Locate every leukocyte (white blood cell).
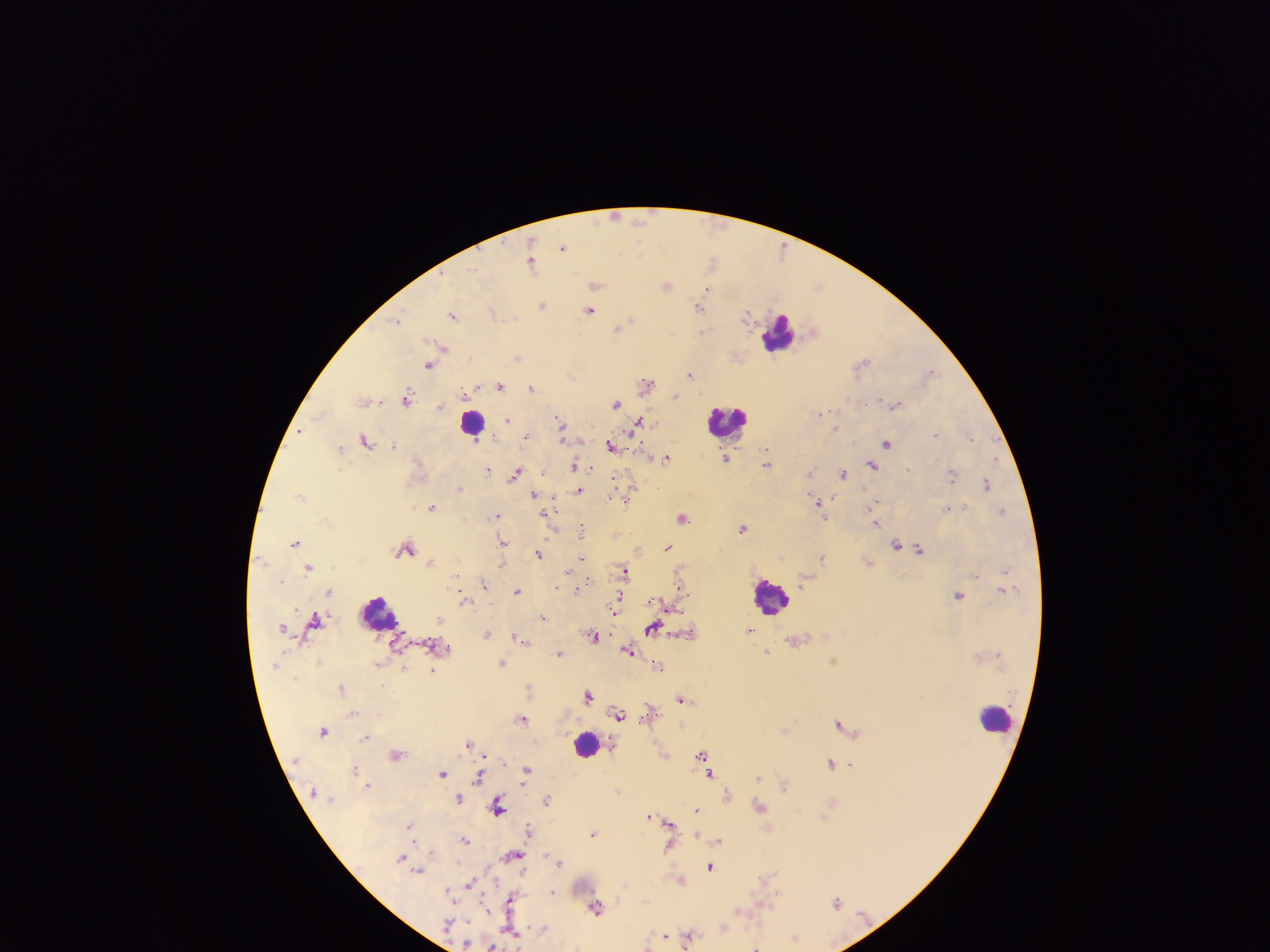

Approximate centers as {x, y} in pixels.
Leukocytes: {780, 333}, {728, 420}, {472, 422}, {770, 596}, {378, 613}, {995, 717}, {585, 744}.

Summary:
  - Plasmodium parasite locations: {616, 215}, {641, 219}, {563, 247}, {641, 252}, {713, 260}, {532, 261}, {595, 285}, {819, 285}, {667, 286}, {708, 289}, {542, 305}, {699, 307}, {589, 310}, {492, 312}, {747, 314}, {453, 315}, {397, 319}, {619, 328}, {704, 330}, {442, 347}, {518, 358}, {862, 362}, {428, 365}, {931, 372}, {690, 373}, {572, 375}, {646, 383}, {500, 386}, {532, 387}, {676, 396}, {408, 398}, {880, 399}, {364, 400}, {616, 403}, {894, 403}, {441, 406}, {820, 414}, {319, 415}, {508, 420}, {560, 422}, {638, 424}, {300, 432}, {936, 434}, {525, 437}, {971, 437}, {564, 438}, {366, 440}, {886, 443}, {395, 445}, {612, 445}, {340, 447}, {647, 456}, {726, 457}, {666, 458}, {995, 459}, {768, 463}, {574, 465}, {872, 466}, {488, 470}, {810, 472}, {542, 473}, {844, 473}, {515, 474}, {952, 474}, {615, 482}, {987, 483}, {631, 486}, {460, 488}, {579, 491}, {300, 494}, {535, 494}, {815, 499}, {818, 504}, {874, 504}, {432, 507}, {948, 508}, {1002, 511}, {496, 516}, {874, 516}, {824, 518}, {683, 519}, {877, 523}, {743, 527}, {581, 528}, {295, 542}, {502, 542}, {896, 544}, {668, 547}, {408, 549}, {639, 550}, {920, 550}, {538, 554}, {581, 558}, {823, 558}, {429, 563}, {502, 564}, {309, 567}, {1006, 570}, {625, 571}, {977, 576}, {484, 584}, {580, 587}, {330, 591}, {517, 591}, {959, 595}, {464, 600}, {653, 601}, {618, 602}, {670, 607}, {439, 618}, {543, 618}, {315, 621}, {282, 626}, {653, 628}, {487, 634}, {593, 636}, {518, 637}, {522, 639}, {629, 650}, {768, 652}, {559, 654}, {502, 664}, {658, 666}, {432, 672}, {341, 687}, {589, 695}, {682, 699}, {649, 711}, {353, 713}, {619, 714}, {522, 718}, {839, 724}, {785, 730}, {324, 731}, {366, 737}, {469, 744}, {396, 754}, {702, 756}, {831, 763}, {851, 764}, {355, 768}, {526, 770}, {443, 773}, {710, 774}, {478, 777}, {758, 778}, {367, 785}, {784, 785}, {727, 795}, {459, 799}, {547, 800}, {498, 806}, {760, 806}, {698, 810}, {650, 816}, {669, 823}, {410, 827}, {530, 830}, {594, 834}, {697, 835}, {465, 840}, {719, 841}, {668, 847}, {430, 850}, {512, 856}, {401, 857}, {559, 861}, {710, 867}, {418, 871}, {680, 880}, {470, 885}, {553, 892}, {511, 900}, {837, 902}, {596, 908}, {739, 911}, {724, 926}, {543, 929}, {512, 933}, {664, 935}, {689, 936}, {795, 936}, {466, 944}, {492, 945}, {756, 946}
  - Country: Ghana
  - Preparation: thick blood film
  - Capture: mobile-phone photograph through a microscope
  - Image size: 1270×952 pixels
  - Field of view: single